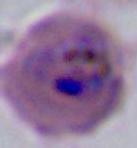 400x or 1000x magnification. Micrograph. A Plasmodium parasite is seen.